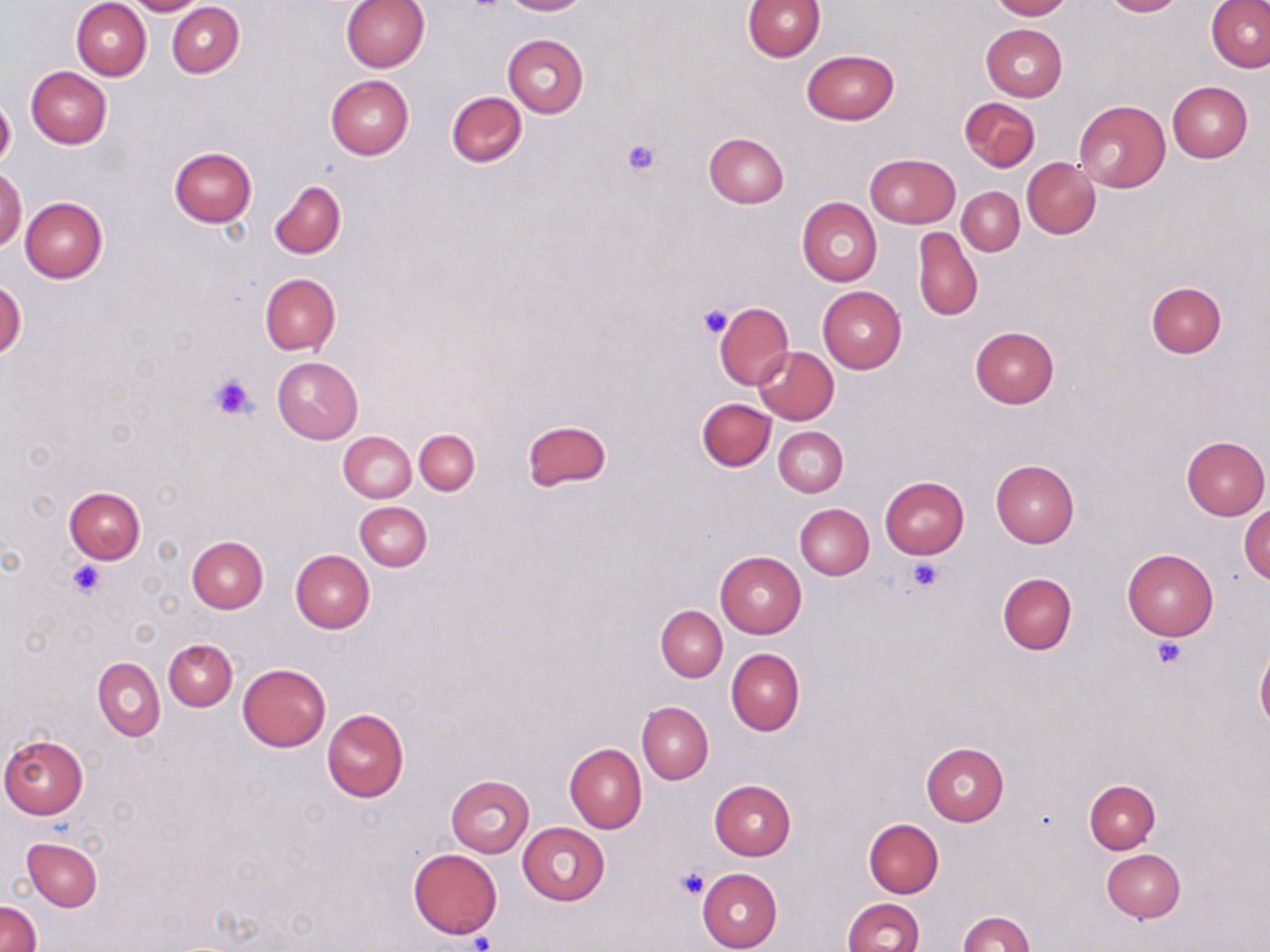

slide_level_diagnosis: no evidence of blood parasites
field_of_view: single
uninfected_red_blood_cell_locations: 'approximate bounding boxes as (x1,y1)-(x2,y2) corner pairs in pixels: (124,0)-(207,15), (341,0)-(429,73), (500,0)-(589,15), (989,0)-(1072,20), (1099,0)-(1184,17), (72,1)-(152,80), (742,1)-(825,62), (167,3)-(244,78), (1207,3)-(1270,72), (981,23)-(1067,100), (503,34)-(588,117), (801,50)-(900,125), (26,66)-(112,148), (325,75)-(413,159), (1168,82)-(1253,162), (447,91)-(527,167), (959,97)-(1039,171), (0,98)-(16,170), (1073,101)-(1170,192), (704,133)-(789,208), (169,147)-(257,226), (866,153)-(960,228), (1022,158)-(1099,239), (0,167)-(26,250), (268,180)-(346,259), (957,187)-(1024,255), (20,197)-(107,282), (797,198)-(882,286), (912,227)-(982,322), (260,274)-(340,355), (0,279)-(26,360), (1146,283)-(1226,358), (818,286)-(906,373), (714,302)-(793,388), (970,328)-(1059,408), (753,346)-(840,424), (272,357)-(363,444), (697,399)-(775,471), (522,419)-(611,492), (774,426)-(848,498), (414,429)-(479,495), (339,431)-(417,502), (1181,436)-(1269,520), (991,460)-(1079,547), (880,477)-(969,559), (64,487)-(146,564), (355,501)-(431,570), (795,503)-(873,579), (1239,505)-(1270,582), (188,536)-(267,614), (1122,549)-(1218,640), (290,551)-(374,633), (715,552)-(806,637), (997,572)-(1077,655), (656,605)-(727,681), (163,638)-(238,710), (1255,644)-(1270,730), (726,649)-(805,735), (94,657)-(165,741), (238,664)-(330,752), (637,702)-(714,784), (321,710)-(410,802), (0,734)-(89,819), (921,743)-(1008,825), (565,744)-(647,833), (445,775)-(535,857), (1084,779)-(1160,853), (709,780)-(796,860), (864,819)-(944,897), (517,822)-(610,906), (22,838)-(101,912), (409,849)-(502,938), (1102,849)-(1185,922), (697,868)-(783,952), (842,898)-(924,952), (0,900)-(41,952), (958,912)-(1034,951)'
preparation: thin blood film
modality: optical microscopy
image_size: 1270×952 pixels
stain: May-Grünwald-Giemsa
magnification: 1000x
platelet_locations: 'approximate bounding boxes as (x1,y1)-(x2,y2) corner pairs in pixels: (621,139)-(660,176), (698,303)-(734,339), (209,373)-(259,421), (906,557)-(945,593), (65,560)-(108,600), (1152,637)-(1187,670), (676,867)-(709,899), (469,931)-(497,951)'